Report the malaria status of this cell.
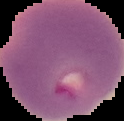
It is parasitized.

Summary:
  - Preparation: thin blood film
  - Image type: segmented cell region on a black background
  - Image size: 124×121 pixels